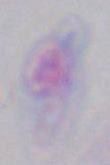
1000x magnification. Micrograph. Toxoplasma gondii is seen.